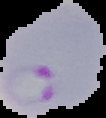

From a thin blood smear. Cell region segmented out of the field of view; the surrounding area is masked to black. Malaria status: parasitized. Image is 106×118 pixels.